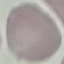
Summary:
  - Malaria status: uninfected
  - Image type: cell patch, automatically extracted from a larger field of view and resized to 64 × 64 pixels
  - Preparation: thin smear
  - Stain: Giemsa
  - Capture: smartphone camera at the microscope eyepiece